Name the blood parasite species.
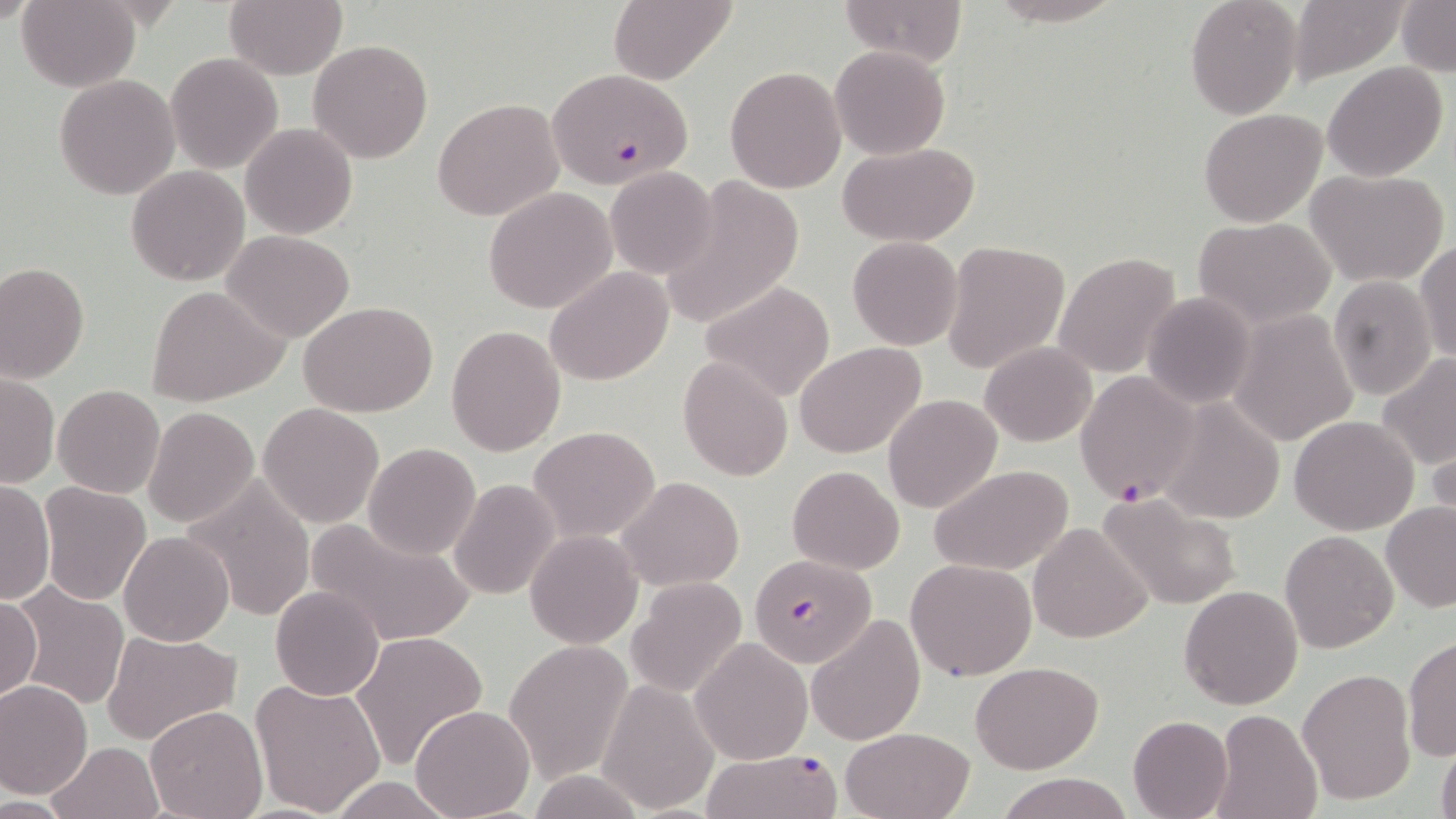

Plasmodium falciparum.

preparation = thin blood smear
uninfected red blood cell locations = approximate bounding boxes as (x1,y1)-(x2,y2) corner pairs in pixels: (17,0)-(141,91), (223,0)-(347,79), (608,0)-(735,85), (835,0)-(968,68), (981,0)-(1124,26), (1184,0)-(1303,118), (1288,0)-(1409,85), (1397,1)-(1456,75), (307,38)-(433,164), (830,46)-(950,159), (165,52)-(284,173), (1323,61)-(1449,182), (725,65)-(847,193), (53,74)-(180,201), (433,99)-(563,221), (1198,108)-(1328,228), (241,123)-(358,239), (835,142)-(983,246), (605,166)-(718,278), (127,167)-(250,285), (1304,167)-(1450,286), (658,178)-(808,327), (484,186)-(618,313), (1194,216)-(1336,327), (221,229)-(356,342), (848,236)-(963,351), (1414,239)-(1456,364), (941,240)-(1070,375), (1050,253)-(1180,376), (0,263)-(89,383), (544,267)-(675,385), (1328,276)-(1438,401), (700,281)-(836,401), (147,285)-(289,408), (1142,292)-(1255,410), (300,301)-(439,418), (1229,310)-(1358,447), (446,324)-(566,456), (797,342)-(927,458), (981,342)-(1096,447), (1376,353)-(1455,471), (678,357)-(792,481), (2,373)-(59,489), (52,385)-(165,499), (882,394)-(1002,513), (1157,397)-(1288,524), (257,403)-(385,530), (142,406)-(259,529), (1290,415)-(1419,534), (527,426)-(660,542), (1427,427)-(1456,539), (363,442)-(481,561), (786,464)-(906,573), (927,465)-(1076,576), (617,476)-(744,590), (181,477)-(317,623), (448,478)-(560,602), (0,480)-(55,606), (38,482)-(153,607), (1102,494)-(1246,610), (1381,502)-(1456,613), (305,518)-(477,645), (1030,521)-(1151,643), (119,530)-(234,646), (525,530)-(643,648), (1279,530)-(1397,653), (905,558)-(1038,681), (626,578)-(748,698), (1178,583)-(1302,710), (10,584)-(131,711), (270,585)-(385,701), (0,594)-(42,705), (806,615)-(925,744), (102,630)-(242,744), (351,630)-(488,771), (1402,635)-(1456,762), (690,636)-(813,765), (502,639)-(634,783), (971,661)-(1103,775), (1296,667)-(1418,804), (596,678)-(720,815), (249,679)-(388,817), (0,681)-(92,798), (410,704)-(534,819), (143,706)-(268,819), (1208,708)-(1324,819), (1127,715)-(1232,819), (839,727)-(973,819), (47,740)-(164,819), (1436,741)-(1456,819), (999,772)-(1132,819), (326,777)-(457,817)
modality = optical microscopy
stain = May-Grünwald-Giemsa
Plasmodium falciparum-infected red blood cell locations = approximate bounding boxes as (x1,y1)-(x2,y2) corner pairs in pixels: (548,69)-(700,196), (1075,370)-(1200,505), (749,554)-(877,668), (700,749)-(842,819)
image size = 1456×819 pixels
field of view = one of a larger specimen
magnification = 1000x